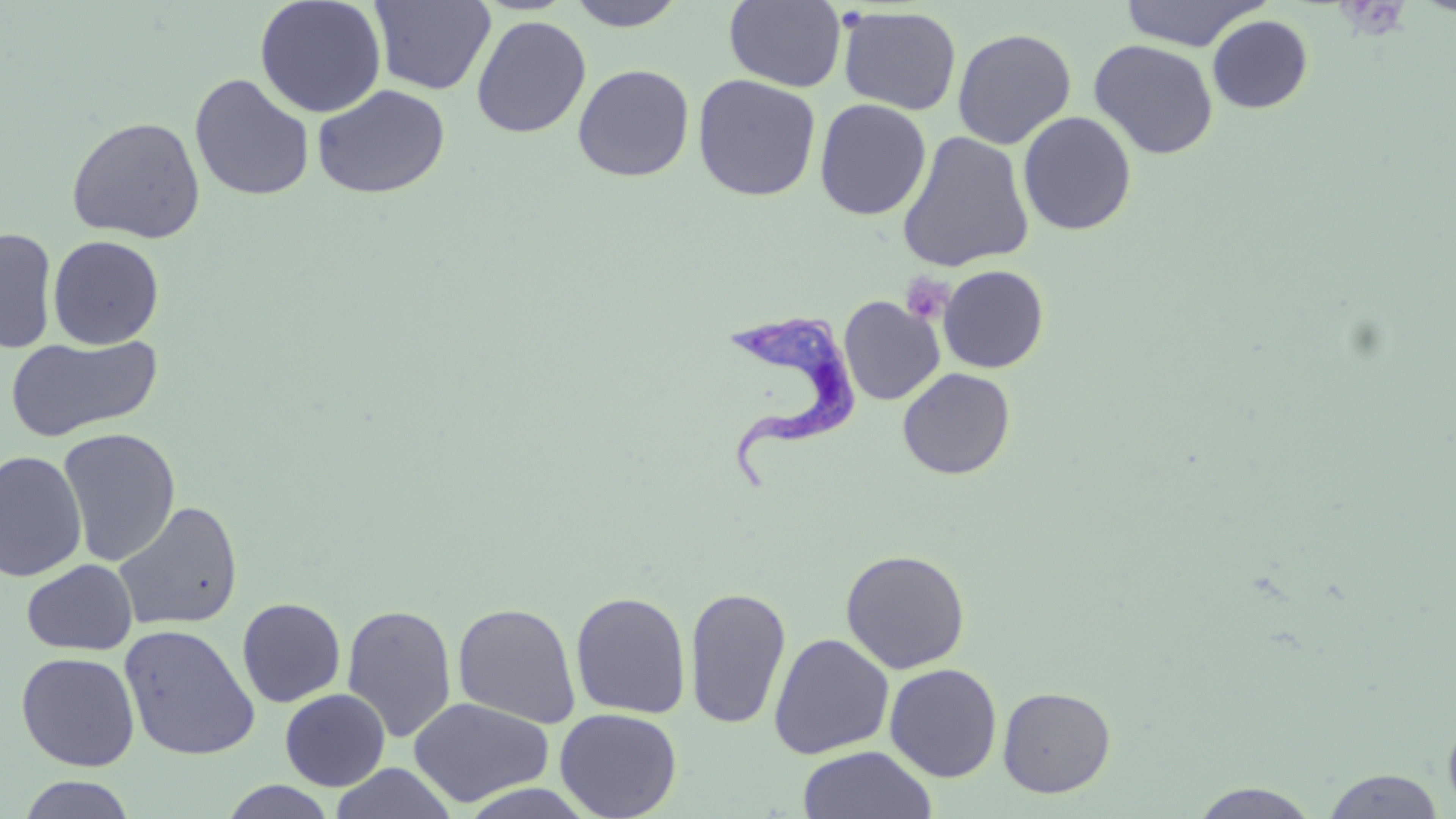

Approximate bounding boxes as [x1, y1, x2, y2] in pixels. Trypanosoma brucei locations: [725, 303, 864, 493]. Platelet locations: [901, 274, 953, 324]. Uninfected red blood cell locations: [254, 0, 387, 118], [564, 0, 687, 30], [369, 1, 496, 95], [724, 1, 846, 92], [1119, 1, 1267, 51], [838, 6, 962, 116], [471, 15, 592, 138], [1207, 15, 1313, 113], [952, 27, 1077, 150], [1089, 40, 1218, 159], [572, 63, 694, 182], [189, 73, 315, 202], [693, 73, 821, 201], [312, 84, 450, 199], [814, 98, 931, 220], [1018, 111, 1136, 236], [66, 116, 205, 243], [897, 130, 1034, 273], [0, 227, 58, 354], [47, 235, 164, 349], [938, 264, 1049, 373], [839, 296, 944, 405], [6, 334, 164, 442], [898, 367, 1016, 480], [58, 428, 181, 566], [0, 450, 87, 583], [113, 501, 243, 632], [840, 549, 971, 674], [22, 560, 138, 655], [684, 585, 792, 731], [570, 590, 692, 719], [237, 598, 345, 707], [452, 602, 581, 727], [341, 603, 458, 743], [119, 623, 260, 760], [768, 633, 895, 759], [16, 652, 140, 772], [884, 662, 1003, 782], [997, 685, 1117, 798], [280, 688, 390, 791], [408, 697, 554, 807], [555, 707, 682, 819], [798, 745, 937, 819], [330, 763, 457, 819], [1321, 768, 1446, 818], [16, 774, 137, 818], [219, 781, 338, 818], [1190, 782, 1322, 818]. Slide-level diagnosis: Trypanosoma brucei. Optical microscopy. Thin blood smear. Captured at 1000x magnification. One field of a larger specimen. May-Grünwald-Giemsa-stained preparation. Image is 1456×819 pixels.